Mark where platelets are.
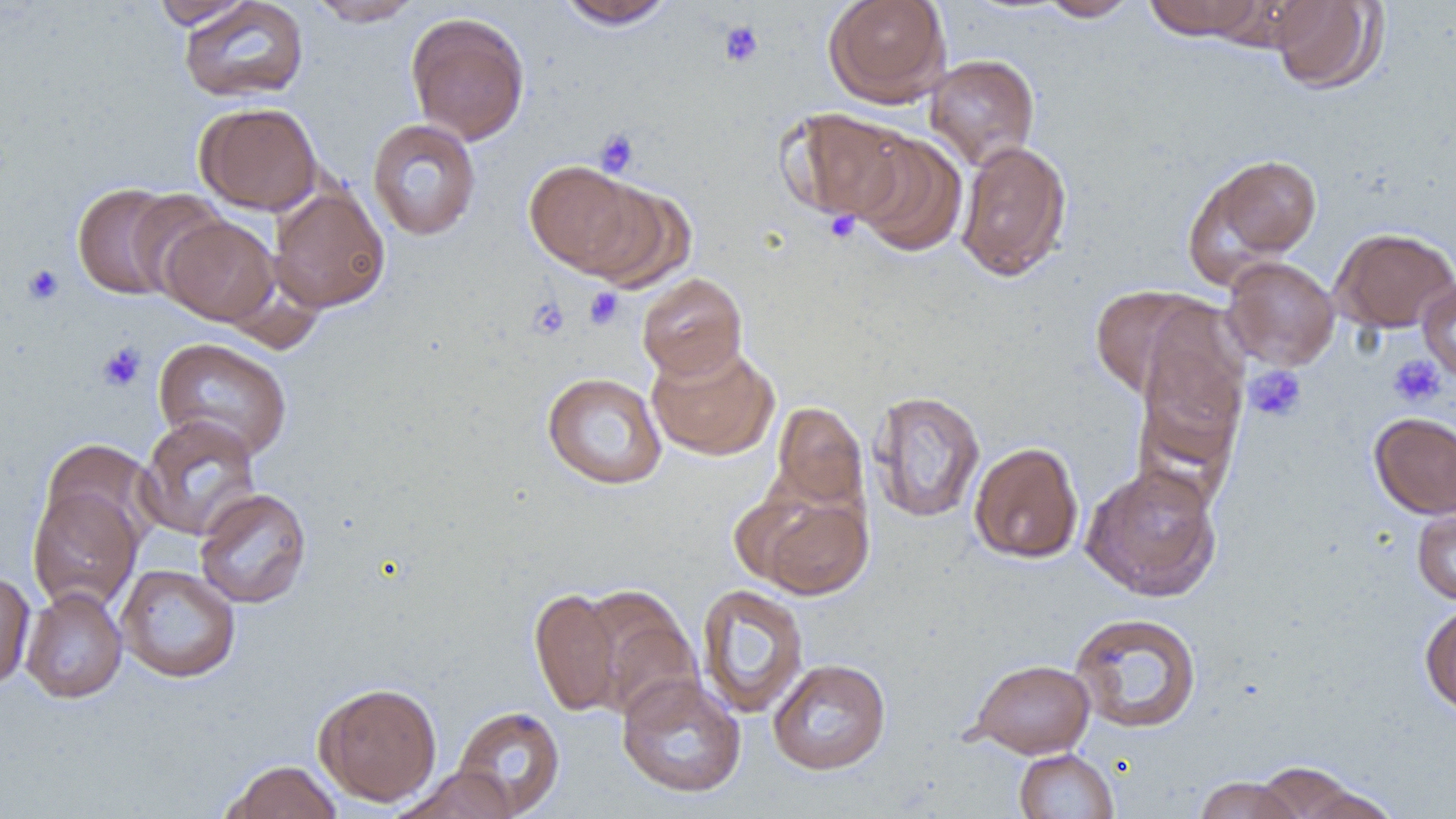

Approximate bounding boxes as (x1,y1)-(x2,y2) corner pairs in pixels.
Platelets: (718,20)-(764,68), (594,129)-(639,176), (823,210)-(860,243), (21,264)-(65,306), (584,287)-(625,330), (527,297)-(570,340), (96,342)-(147,392), (1388,354)-(1446,407), (1245,364)-(1307,422).

slide-level diagnosis = negative for blood parasites
modality = light microscopy
magnification = 1000x
image size = 1456×819 pixels
uninfected red blood cell locations = approximate bounding boxes as (x1,y1)-(x2,y2) corner pairs in pixels: (150,0)-(255,29), (178,0)-(309,103), (307,0)-(424,26), (556,0)-(676,30), (823,0)-(951,107), (1037,0)-(1141,21), (1144,0)-(1261,41), (1269,0)-(1386,94), (1207,1)-(1326,52), (405,12)-(530,146), (925,54)-(1040,170), (195,101)-(323,215), (781,108)-(913,224), (367,118)-(482,241), (851,132)-(967,257), (955,140)-(1073,281), (1188,153)-(1322,280), (523,160)-(650,277), (71,182)-(191,302), (579,182)-(698,293), (269,184)-(390,313), (124,189)-(233,300), (160,214)-(280,326), (1332,227)-(1456,333), (1221,256)-(1340,371), (637,273)-(747,380), (1417,279)-(1456,384), (1089,285)-(1219,402), (1133,332)-(1248,476), (153,337)-(293,461), (646,342)-(778,461), (541,372)-(667,489), (868,390)-(985,523), (771,401)-(868,512), (1369,412)-(1456,519), (136,415)-(263,541), (39,439)-(159,549), (969,441)-(1084,563), (1081,462)-(1223,602), (28,486)-(142,613), (194,488)-(312,608), (750,492)-(873,600), (1412,506)-(1456,604), (116,564)-(241,683), (0,570)-(35,691), (696,583)-(809,719), (20,587)-(128,703), (530,587)-(624,716), (579,587)-(702,723), (1419,602)-(1456,716), (1069,611)-(1203,733), (768,658)-(891,775), (968,658)-(1095,758), (617,673)-(746,798), (314,681)-(443,806), (451,705)-(566,817), (1014,748)-(1119,819), (220,759)-(342,819), (1253,761)-(1364,818), (391,767)-(519,819), (1193,776)-(1304,819), (1296,785)-(1402,819)
field of view = one of a larger specimen
preparation = thin blood film